Locate every malaria parasite.
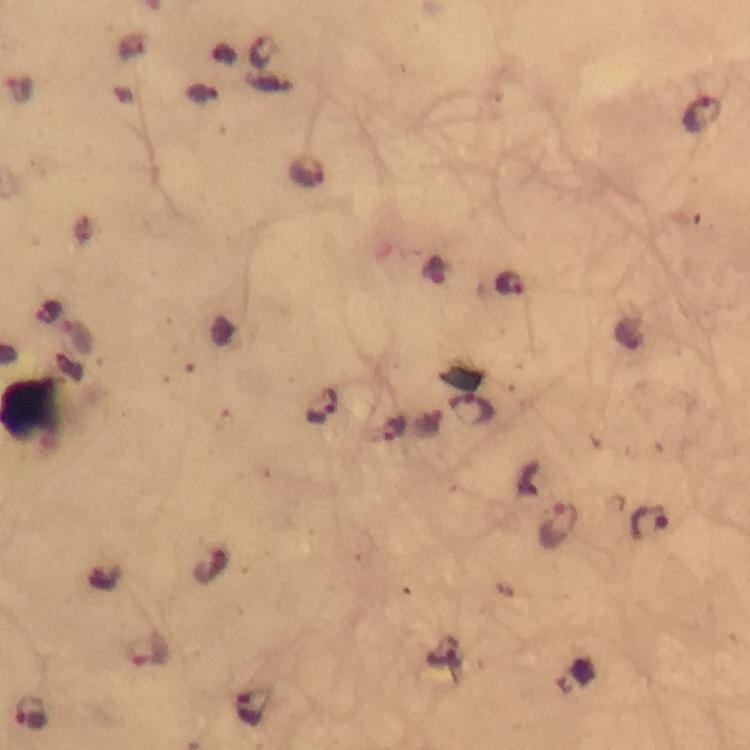
Approximate centers as (x, y) in pixels.
Malaria parasites: (262, 49), (702, 113), (307, 171), (435, 270), (509, 283), (77, 338), (323, 405), (473, 411), (390, 429), (649, 521), (559, 526), (106, 578), (149, 648), (446, 653), (254, 710), (31, 713).

Summary:
  - Preparation: thick blood film
  - Capture: smartphone mounted on the microscope
  - Image size: 750×750 pixels
  - Cropped from: one field of view
  - Magnification: 100x
  - Immersion oil: applied
  - Context: from a malaria diagnostic workup
  - Stain: Giemsa